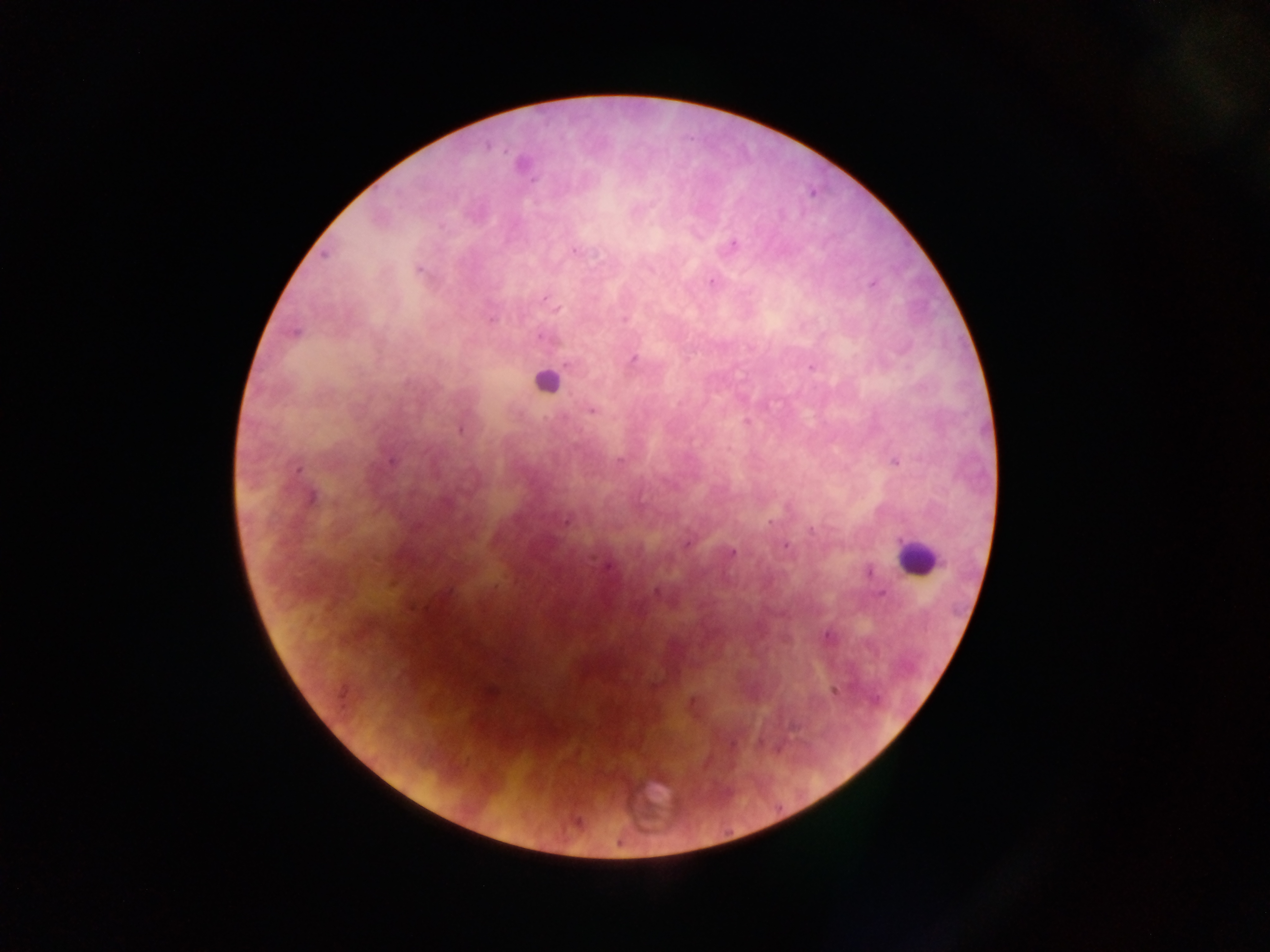 Approximate centers as x y in pixels. Plasmodium parasite locations: 488 147; 523 165; 733 245; 575 251; 325 255; 418 270; 711 282; 871 284; 548 301; 556 308; 491 319; 624 319; 294 332; 542 338; 633 359; 568 365; 811 367; 592 410; 461 430; 393 461; 618 461; 895 462; 299 468; 312 497; 566 522; 770 522; 811 530; 686 544; 785 547; 732 552; 608 567; 870 572; 448 592; 656 592; 880 594; 827 636; 491 690; 835 690; 875 699; 577 822. Leukocyte locations: 546 380; 916 556; 652 803. Single field of view. Image is 1270×952 pixels. Photographed through a microscope with a mobile-phone camera. Collected in Ghana. Thick blood smear.